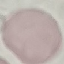

{
  "malaria_status": "uninfected",
  "stain": "Giemsa",
  "image_type": "cell patch, automatically extracted from a larger field of view and resized to 64 × 64 pixels",
  "preparation": "thin blood smear",
  "capture": "smartphone camera at the microscope eyepiece"
}